Identify the cell.
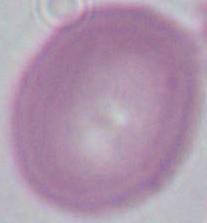

An erythrocyte.

Summary:
  - Modality: photomicrograph
  - Magnification: 1000x